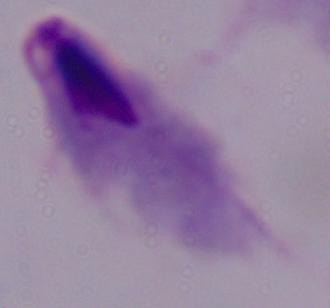
modality = micrograph
magnification = 1000x
identification = trichomonad